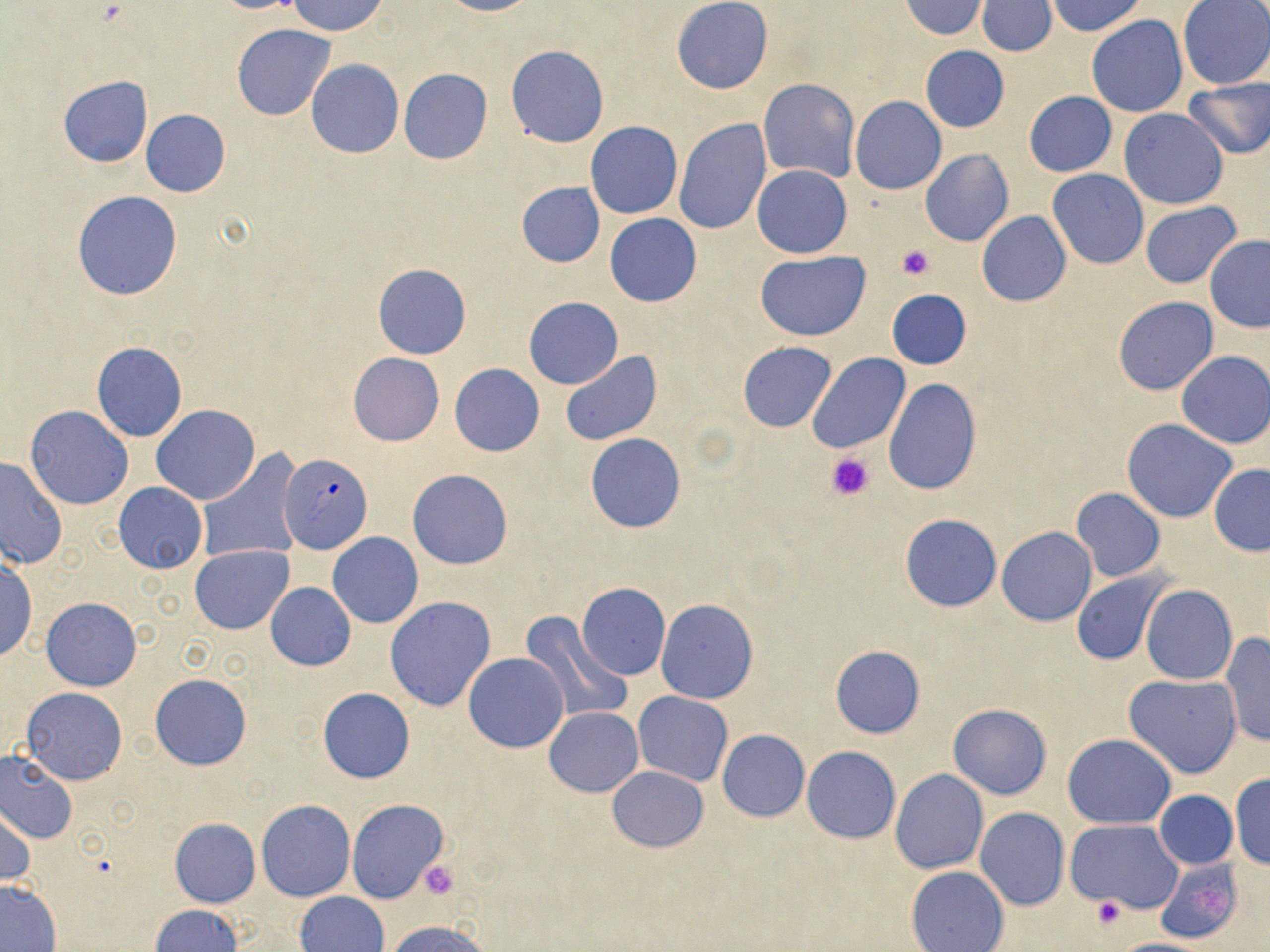
Summary:
  - Coordinate format: approximate bounding boxes as (x1,y1)-(x2,y2) corner pairs in pixels
  - Plasmodium falciparum-infected red blood cell locations: (278,453)-(372,554)
  - Platelet locations: (896,246)-(936,281), (827,450)-(874,500), (416,860)-(460,901), (1091,897)-(1126,927)
  - Uninfected red blood cell locations: (209,0)-(307,14), (437,0)-(534,16), (672,0)-(773,93), (902,0)-(987,40), (1045,0)-(1147,37), (286,1)-(388,37), (976,1)-(1056,56), (1178,1)-(1270,90), (1087,15)-(1189,118), (231,24)-(337,122), (505,45)-(608,147), (920,46)-(1009,133), (306,60)-(404,157), (399,68)-(492,164), (58,76)-(152,168), (1182,78)-(1270,160), (759,79)-(859,182), (1023,91)-(1117,176), (850,96)-(947,195), (1119,107)-(1227,209), (141,109)-(229,197), (674,120)-(772,236), (585,122)-(682,219), (1094,142)-(1224,246), (920,149)-(1014,247), (752,165)-(852,257), (1047,169)-(1148,269), (517,181)-(605,267), (72,191)-(183,300), (1141,202)-(1242,290), (976,210)-(1071,307), (605,214)-(701,306), (1205,234)-(1269,332), (755,251)-(870,341), (372,263)-(471,359), (887,289)-(971,369), (1113,296)-(1218,395), (524,297)-(623,389), (737,340)-(837,432), (91,342)-(187,443), (1176,351)-(1270,448), (560,352)-(662,447), (806,352)-(909,455), (347,353)-(444,446), (449,364)-(545,457), (884,378)-(981,495), (26,405)-(133,510), (151,406)-(260,505), (1122,418)-(1238,522), (586,432)-(685,532), (196,452)-(304,564), (1,457)-(68,569), (1208,464)-(1270,557), (407,469)-(514,570), (113,483)-(207,573), (1072,488)-(1165,581), (900,514)-(1001,612), (996,525)-(1097,626), (328,532)-(424,628), (191,544)-(293,634), (0,559)-(37,663), (1072,572)-(1170,665), (265,582)-(356,671), (576,583)-(671,681), (1141,585)-(1237,684), (384,596)-(497,712), (41,597)-(141,690), (655,599)-(757,704), (517,612)-(631,725), (1220,632)-(1269,746), (830,646)-(925,739), (464,652)-(569,753), (150,674)-(252,770), (1124,674)-(1243,778), (21,686)-(126,785), (318,687)-(416,783), (633,691)-(733,786), (948,704)-(1052,799), (544,707)-(643,797), (717,730)-(809,821), (1063,734)-(1177,829), (802,746)-(901,843), (0,749)-(78,845), (606,766)-(708,852), (890,770)-(988,874), (1229,771)-(1270,870), (1153,790)-(1237,869), (257,800)-(355,902), (348,800)-(449,904), (1,805)-(35,888), (975,808)-(1069,911), (170,818)-(260,907), (1067,819)-(1184,914), (1154,856)-(1245,944), (905,865)-(1009,951), (0,881)-(61,950), (295,892)-(389,952), (150,905)-(242,952), (388,919)-(489,952), (1106,938)-(1218,952)
  - Slide-level diagnosis: Plasmodium falciparum
  - Preparation: thin blood smear
  - Image size: 1270×952 pixels
  - Stain: May-Grünwald-Giemsa
  - Field of view: single
  - Magnification: 1000x
  - Modality: optical microscopy